Give the preparation type.
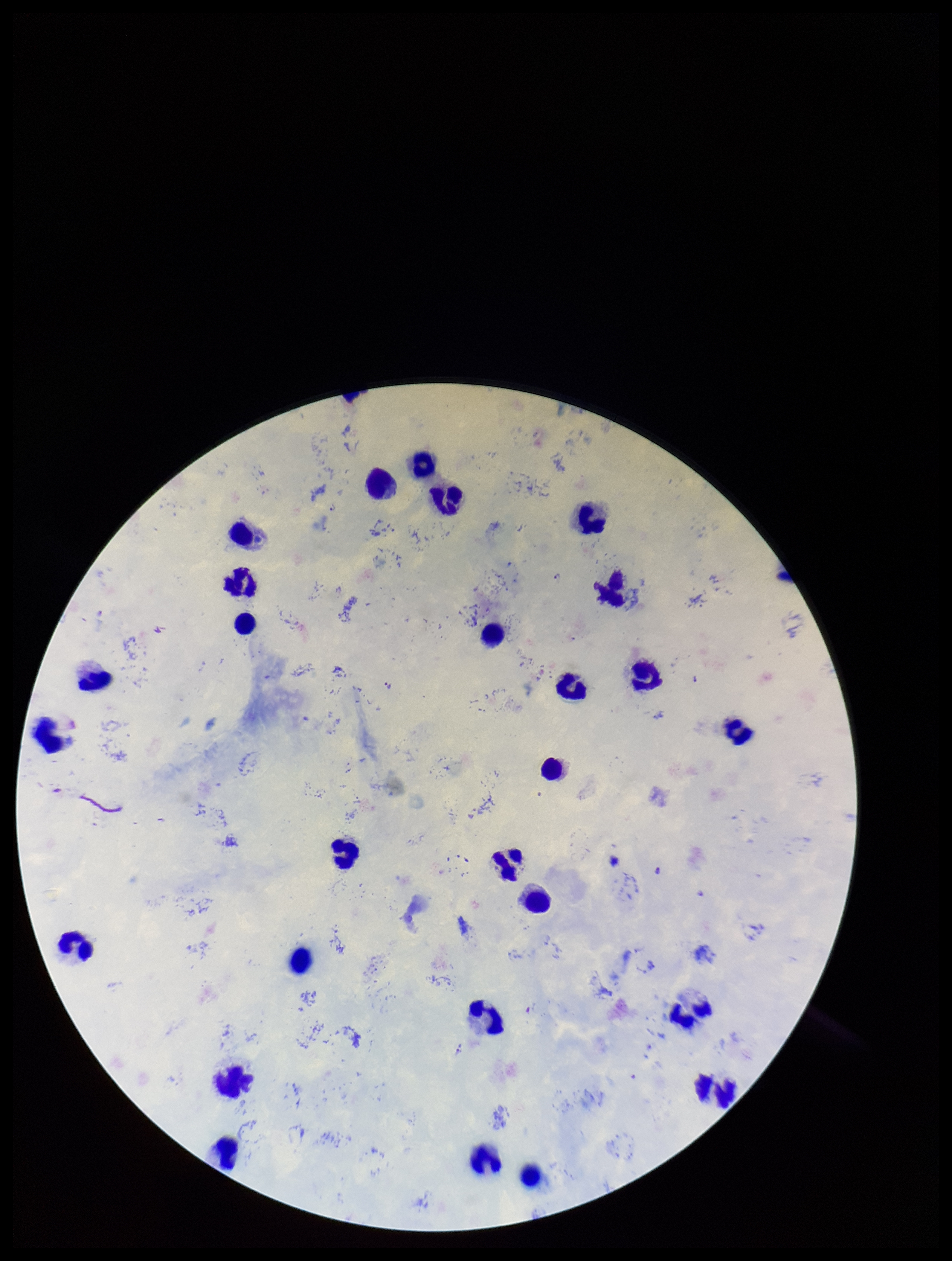

It is a thick blood smear.

Giemsa stain. Parasite count: 5. Plasmodium parasites: identified. Patient malaria status: infected. Single field of view. Photographed through the microscope eyepiece with a smartphone camera. Image is 952×1261 pixels. Leukocyte count: 27. Species reported for this patient: Plasmodium falciparum.